Comment on the morphology of the red blood cells.
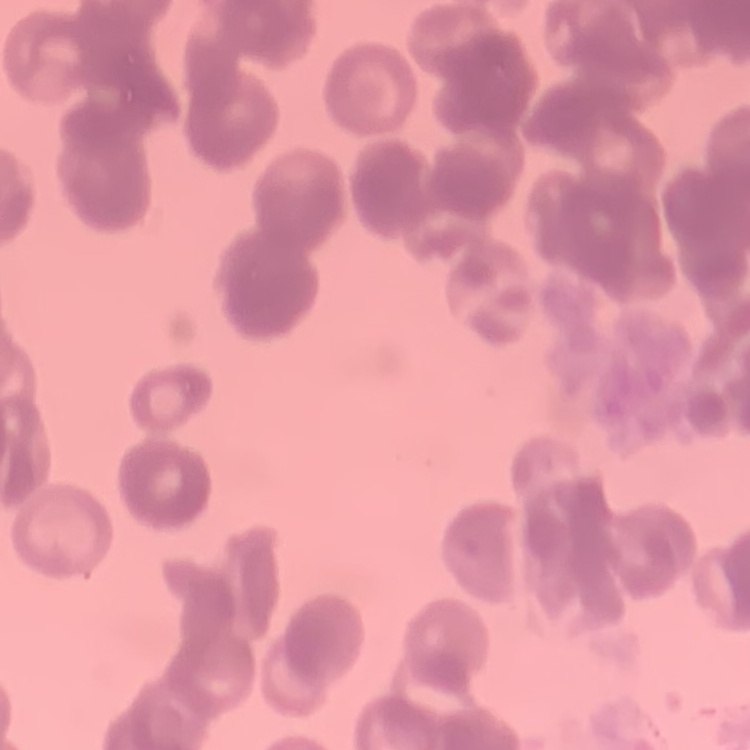

They show rouleaux formation.

preparation: thin blood film
stain: Field's or Giemsa
image_type: one tile cut from a larger photomicrograph